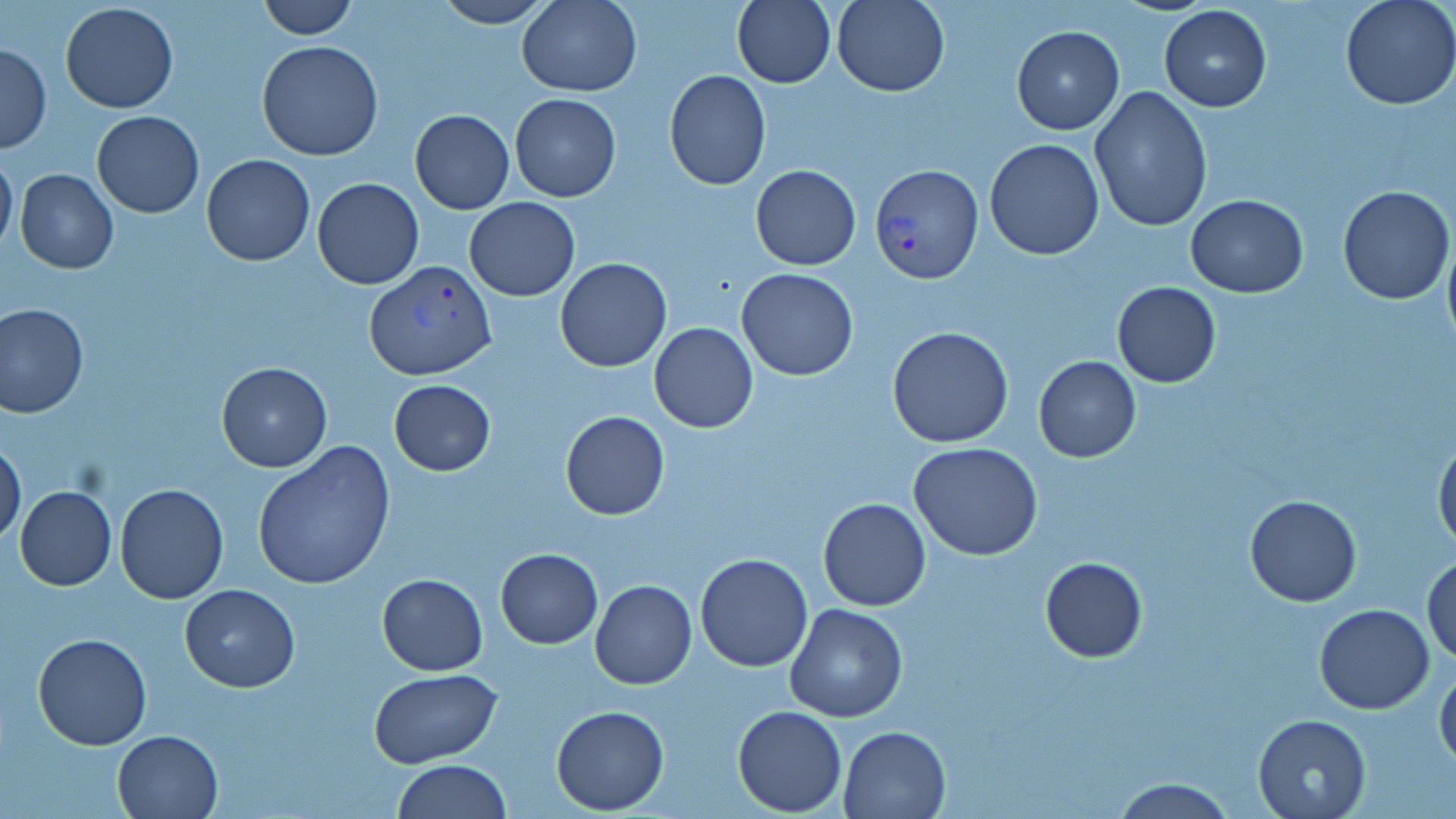

Summary:
  - Coordinate format: approximate bounding boxes as (x1, y1, x2, y2) in pixels
  - Plasmodium vivax-infected red blood cell locations: (868, 164, 986, 285), (364, 260, 497, 381)
  - Uninfected red blood cell locations: (256, 0, 358, 38), (433, 0, 555, 27), (516, 0, 642, 96), (832, 0, 950, 96), (1338, 0, 1456, 109), (731, 1, 836, 87), (59, 2, 179, 114), (1157, 4, 1271, 114), (1011, 25, 1125, 134), (257, 40, 384, 161), (0, 44, 50, 152), (665, 69, 771, 189), (1089, 86, 1213, 232), (509, 94, 622, 203), (409, 110, 514, 213), (92, 111, 203, 218), (985, 138, 1104, 260), (0, 150, 17, 260), (201, 154, 315, 267), (751, 165, 860, 269), (15, 170, 118, 274), (312, 177, 424, 289), (1337, 185, 1453, 303), (1184, 195, 1308, 298), (464, 198, 580, 300), (1442, 226, 1456, 354), (555, 257, 672, 372), (736, 268, 859, 380), (1112, 282, 1221, 388), (0, 304, 89, 418), (648, 322, 759, 433), (886, 326, 1014, 448), (1033, 356, 1141, 462), (216, 360, 333, 473), (388, 379, 496, 476), (560, 411, 670, 520), (1434, 435, 1456, 554), (0, 441, 27, 548), (908, 443, 1043, 562), (253, 444, 395, 589), (115, 483, 228, 603), (15, 485, 117, 591), (1244, 494, 1362, 607), (818, 498, 930, 612), (495, 548, 603, 648), (695, 553, 814, 672), (1423, 553, 1456, 664), (1039, 556, 1147, 662), (376, 573, 488, 674), (590, 579, 696, 689), (179, 583, 302, 692), (784, 603, 909, 722), (1315, 603, 1434, 714), (32, 634, 153, 751), (1434, 663, 1456, 769), (369, 669, 501, 768), (552, 705, 670, 813), (732, 705, 847, 816), (1253, 714, 1371, 819), (839, 726, 950, 818), (113, 729, 222, 817), (392, 760, 510, 818), (1113, 777, 1233, 818)
  - Slide-level diagnosis: Plasmodium vivax
  - Magnification: 1000x
  - Modality: light microscopy
  - Preparation: thin blood film
  - Stain: May-Grünwald-Giemsa
  - Field of view: one of a larger specimen
  - Image size: 1456×819 pixels